Locate and identify every blood parasite.
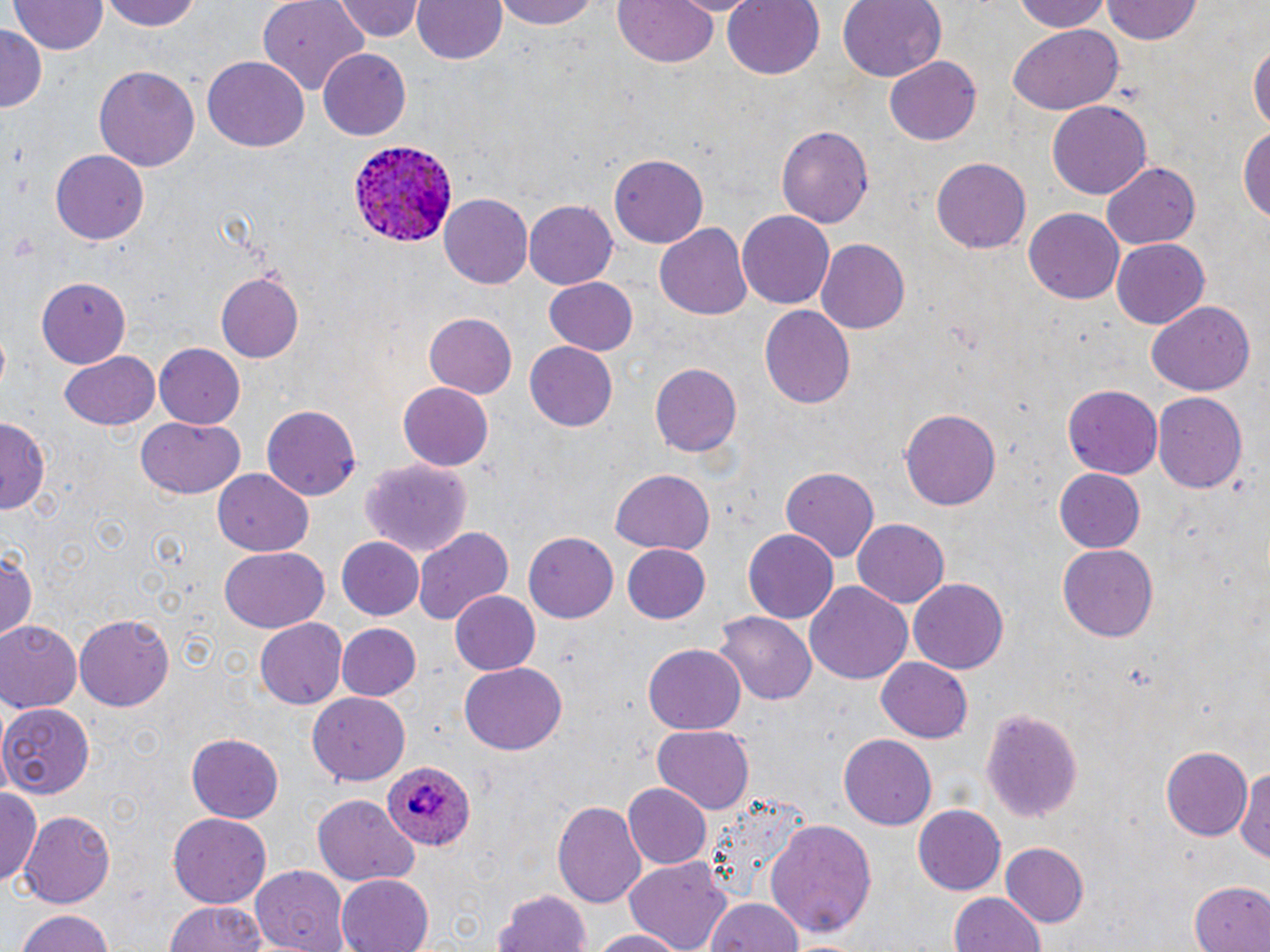

Approximate bounding boxes as [x1, y1, x2, y2] in pixels.
Plasmodium ovale-infected red blood cells: [351, 141, 459, 250], [385, 755, 475, 851].
No Plasmodium falciparum, Plasmodium malariae, Plasmodium vivax, Babesia divergens, or Trypanosoma brucei observed.

Summary:
  - Uninfected red blood cell locations: [102, 0, 203, 31], [258, 0, 372, 90], [332, 0, 425, 42], [413, 0, 506, 65], [498, 0, 604, 29], [722, 0, 824, 79], [838, 0, 945, 83], [1010, 0, 1113, 32], [10, 1, 106, 55], [609, 1, 723, 70], [1102, 2, 1202, 45], [0, 27, 45, 111], [1009, 28, 1122, 113], [1250, 38, 1269, 141], [318, 50, 411, 140], [203, 57, 309, 152], [885, 57, 980, 146], [95, 65, 200, 173], [1048, 98, 1152, 199], [775, 124, 875, 228], [1238, 126, 1270, 227], [49, 151, 151, 245], [609, 154, 708, 247], [930, 156, 1031, 251], [1101, 162, 1199, 250], [439, 193, 532, 286], [525, 198, 620, 290], [1024, 207, 1123, 302], [738, 211, 834, 309], [655, 222, 753, 317], [1111, 237, 1211, 330], [816, 238, 910, 334], [216, 272, 304, 361], [545, 276, 638, 355], [37, 279, 132, 367], [1146, 300, 1255, 398], [760, 304, 855, 410], [422, 313, 517, 399], [524, 340, 620, 431], [155, 343, 246, 426], [58, 351, 161, 430], [649, 361, 740, 459], [397, 382, 494, 470], [1062, 385, 1163, 479], [1152, 390, 1247, 490], [263, 405, 361, 499], [900, 410, 1002, 508], [0, 416, 49, 514], [137, 416, 247, 499], [361, 458, 472, 555], [781, 465, 881, 561], [213, 467, 313, 556], [611, 469, 715, 553], [1055, 469, 1145, 552], [852, 518, 949, 608], [414, 525, 516, 624], [741, 527, 839, 623], [523, 530, 618, 623], [335, 536, 424, 621], [621, 541, 714, 624], [1058, 543, 1158, 640], [0, 545, 38, 646], [220, 547, 329, 632], [908, 577, 1010, 673], [804, 581, 914, 686], [449, 590, 542, 674], [714, 611, 816, 706], [73, 613, 175, 711], [254, 618, 348, 709], [1, 620, 82, 712], [333, 622, 421, 701], [642, 645, 746, 734], [875, 657, 974, 743], [460, 664, 568, 753], [309, 692, 410, 785], [0, 704, 96, 799], [980, 706, 1084, 823], [652, 723, 756, 813], [186, 734, 282, 822], [838, 734, 937, 831], [1158, 742, 1254, 841], [1238, 761, 1270, 868], [623, 782, 714, 870], [1, 789, 42, 889], [700, 791, 811, 906], [312, 797, 419, 886], [552, 800, 645, 911], [914, 804, 1006, 894], [18, 808, 117, 907], [167, 812, 273, 907], [765, 818, 878, 942], [998, 843, 1090, 927], [624, 856, 734, 951], [249, 865, 351, 951], [334, 874, 434, 952], [1189, 882, 1269, 952], [494, 889, 594, 952], [947, 891, 1046, 952], [702, 897, 804, 952], [162, 899, 274, 952], [13, 908, 119, 952], [589, 927, 692, 951]
  - Slide-level diagnosis: Plasmodium ovale
  - Modality: light microscopy
  - Preparation: thin blood smear
  - Field of view: single
  - Magnification: 1000x
  - Stain: May-Grünwald-Giemsa
  - Image size: 1270×952 pixels